Point out each Plasmodium parasite.
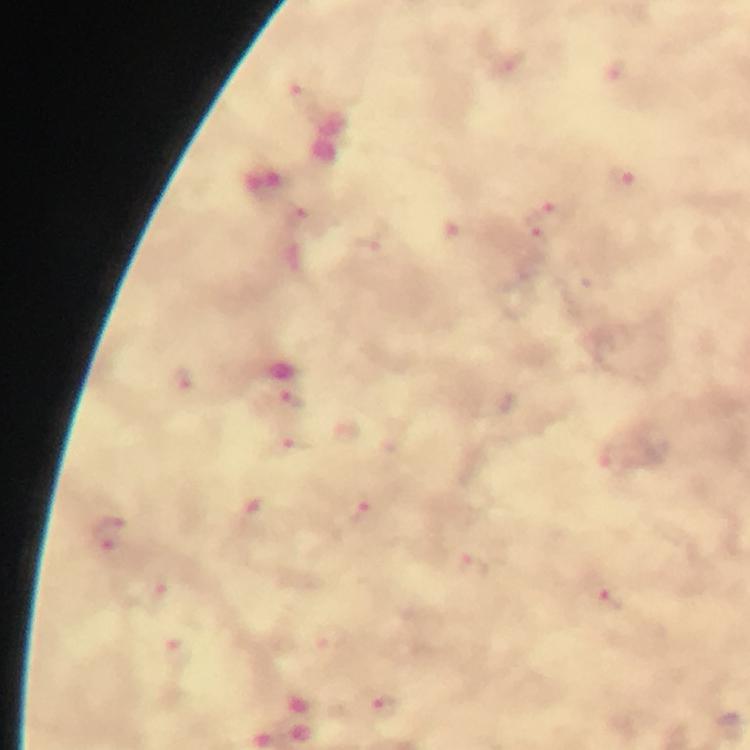
Approximate object centers, in pixels from the top-left corner.
Plasmodium parasites: (x=307, y=101), (x=625, y=178), (x=543, y=220), (x=182, y=382), (x=293, y=400), (x=296, y=443), (x=361, y=513), (x=109, y=534), (x=475, y=567), (x=616, y=600), (x=386, y=709).

{
  "context": "from a diagnostic examination for malaria",
  "preparation": "thick blood smear",
  "immersion_oil": "applied",
  "stain": "Giemsa",
  "cropped_from": "one field of view",
  "magnification": "100x",
  "image_size": "750×750 pixels",
  "capture": "smartphone photograph through a microscope"
}